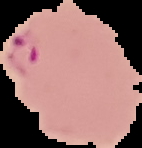

image type = segmented cell region with the area outside set to black
preparation = thin blood smear
result = malaria parasites detected
image size = 142×148 pixels